Comment on the morphology of the erythrocytes.
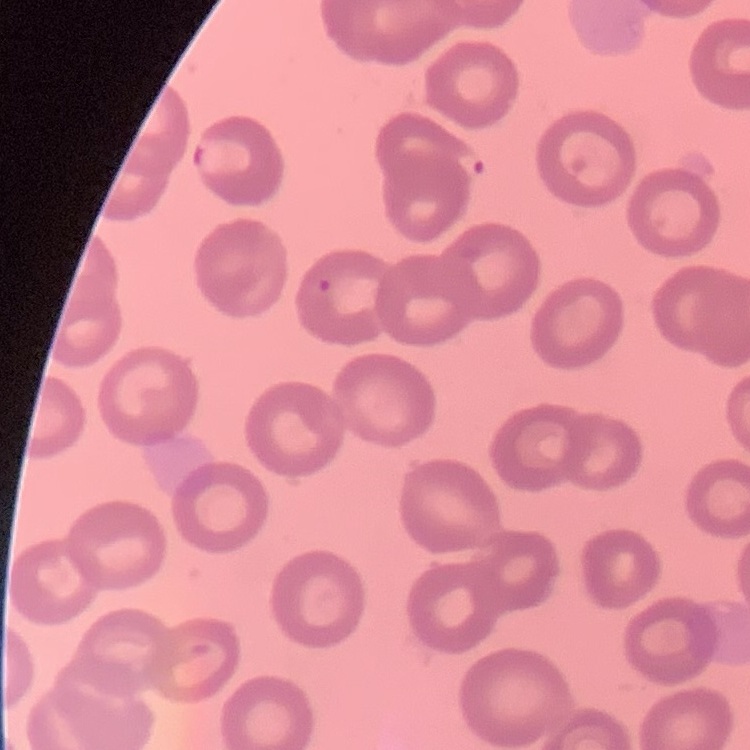

They show no rouleaux formation.

Summary:
  - Image type: square crop of a larger photomicrograph
  - Preparation: thin blood film
  - Stain: Field's or Giemsa